Classify this cell by malaria status.
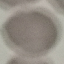

It is uninfected.

preparation = thin blood film
stain = Giemsa
capture = smartphone camera at the microscope eyepiece
image type = cell patch, automatically extracted from a larger field of view and resized to 64 × 64 pixels